Report the malaria status of this cell.
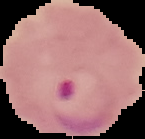

It is parasitized.

From a thin blood smear. Image is 145×139 pixels. The area outside the segmented cell region is set to black.